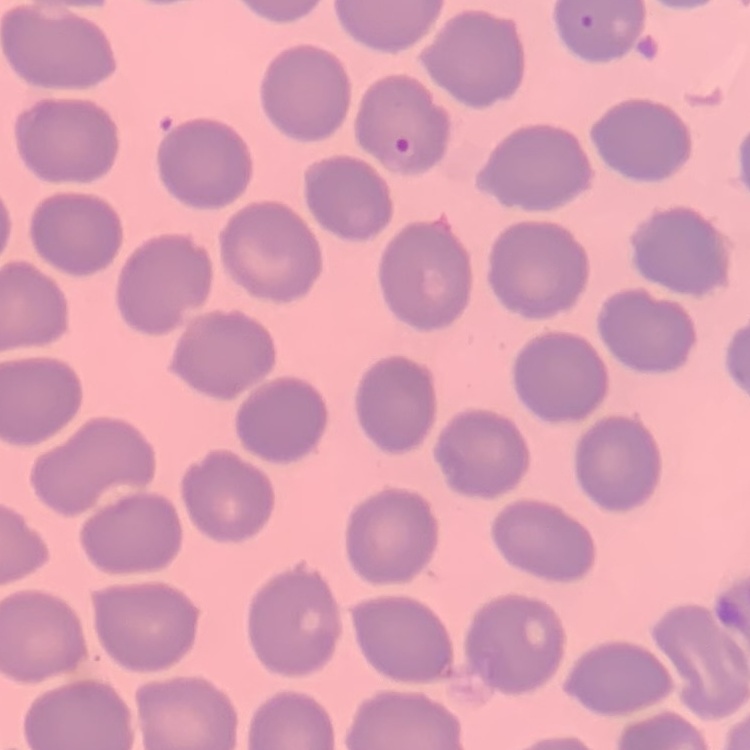
Summary:
  - Red blood cell morphology: no rouleaux formation
  - Preparation: thin blood smear
  - Image type: square crop of a larger photomicrograph
  - Stain: Field's or Giemsa